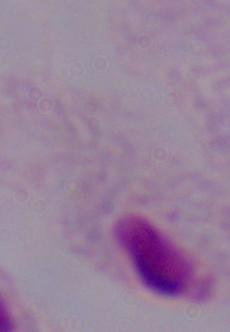 Captured at 1000x magnification. A trichomonad is seen. Photomicrograph.